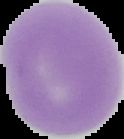

malaria status = uninfected
image type = segmented cell region with the area outside set to black
image size = 124×139 pixels
preparation = thin blood smear